Name the parasite shown.
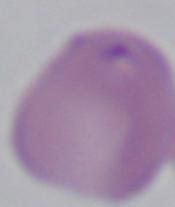
This is Babesia.

1000x magnification. Photomicrograph.